Locate every malaria parasite.
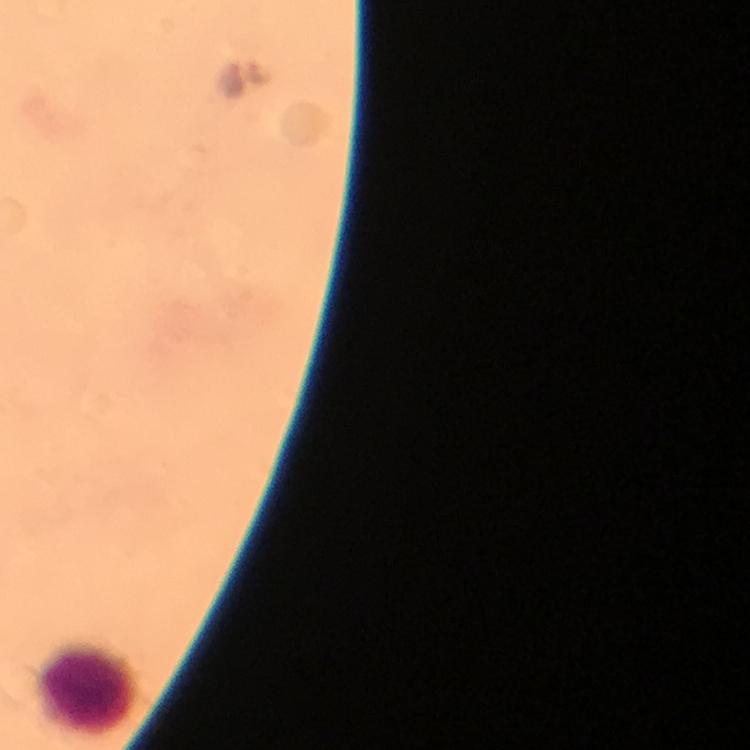
No malaria parasites detected.

Approximate centers as (x, y) in pixels. Leukocyte locations: (87, 687). Cropped region of a single field of view. Immersion oil was used. Photographed through the microscope with a smartphone camera. From a diagnostic examination for malaria. 100x magnification. Image is 750×750 pixels. Giemsa-stained preparation. Thick blood film.